Identify the parasite.
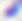

This is Toxoplasma gondii.

modality = micrograph
magnification = 400x